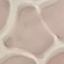
Result: no malaria parasites detected. Photographed with a smartphone camera at the microscope eyepiece. Thin smear of blood. Cell patch, automatically extracted from a larger field of view and resized to 64 × 64 pixels. Giemsa stain.